Report the malaria status of this cell.
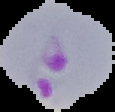
Parasitized.

image type = segmented cell region with the area outside set to black
preparation = thin blood film
image size = 115×112 pixels